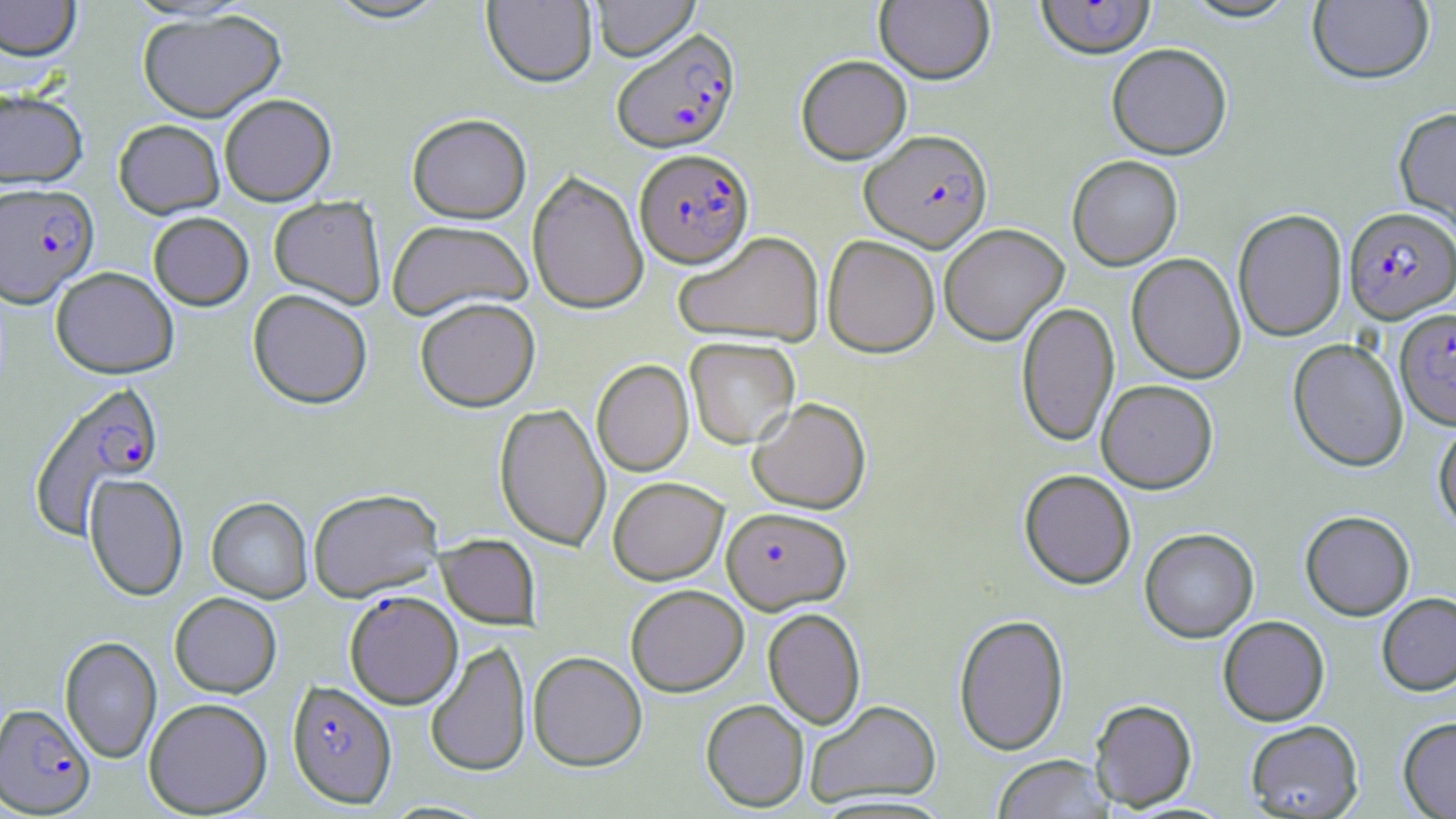
Summary:
  - Coordinate format: approximate bounding boxes as (x1,y1)-(x2,y2) corner pairs in pixels
  - Plasmodium falciparum-infected red blood cell locations: (1035,0)-(1157,61), (611,28)-(741,153), (859,130)-(993,252), (634,148)-(755,268), (0,182)-(99,307), (1344,206)-(1456,322), (1395,307)-(1456,430), (28,382)-(166,538), (721,506)-(852,614), (345,590)-(463,709), (286,680)-(397,808), (0,703)-(95,816)
  - Uninfected red blood cell locations: (0,0)-(81,62), (324,0)-(449,24), (590,0)-(700,61), (874,0)-(995,84), (1180,0)-(1301,23), (482,1)-(598,87), (1308,1)-(1434,86), (137,8)-(287,122), (1106,44)-(1233,160), (795,55)-(912,164), (0,88)-(89,188), (219,93)-(337,205), (1394,107)-(1456,234), (407,113)-(531,223), (113,119)-(225,218), (1067,155)-(1183,270), (527,170)-(649,315), (268,196)-(387,309), (1232,209)-(1348,342), (148,212)-(254,310), (386,219)-(533,321), (938,224)-(1069,346), (672,231)-(824,347), (822,234)-(940,358), (1126,252)-(1246,384), (51,266)-(179,378), (248,289)-(373,409), (415,297)-(540,412), (1016,301)-(1119,448), (684,337)-(800,449), (1288,339)-(1408,473), (592,359)-(693,477), (1096,379)-(1218,493), (747,397)-(872,513), (494,402)-(611,552), (1433,420)-(1456,535), (1019,469)-(1136,590), (83,474)-(189,601), (608,476)-(728,585), (308,488)-(442,601), (207,497)-(313,602), (1300,511)-(1415,621), (1139,528)-(1259,643), (435,534)-(541,628), (625,584)-(749,696), (169,592)-(282,697), (1377,593)-(1456,697), (762,608)-(866,729), (953,613)-(1069,756), (1218,616)-(1330,726), (59,635)-(162,764), (425,641)-(531,777), (528,651)-(647,771), (143,697)-(272,817), (1089,698)-(1198,812), (700,699)-(809,812), (804,699)-(942,808), (1398,717)-(1456,818), (1245,720)-(1363,818), (992,754)-(1113,819)
  - Slide-level diagnosis: Plasmodium falciparum
  - Field of view: single
  - Stain: May-Grünwald-Giemsa
  - Modality: light microscopy
  - Image size: 1456×819 pixels
  - Magnification: 1000x
  - Preparation: thin blood smear